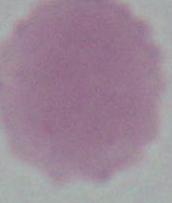

Summary:
  - Identification: red blood cell
  - Magnification: 1000x
  - Modality: micrograph